Give the position of every Plasmodium falciparum parasite, noting its life-cycle stage.
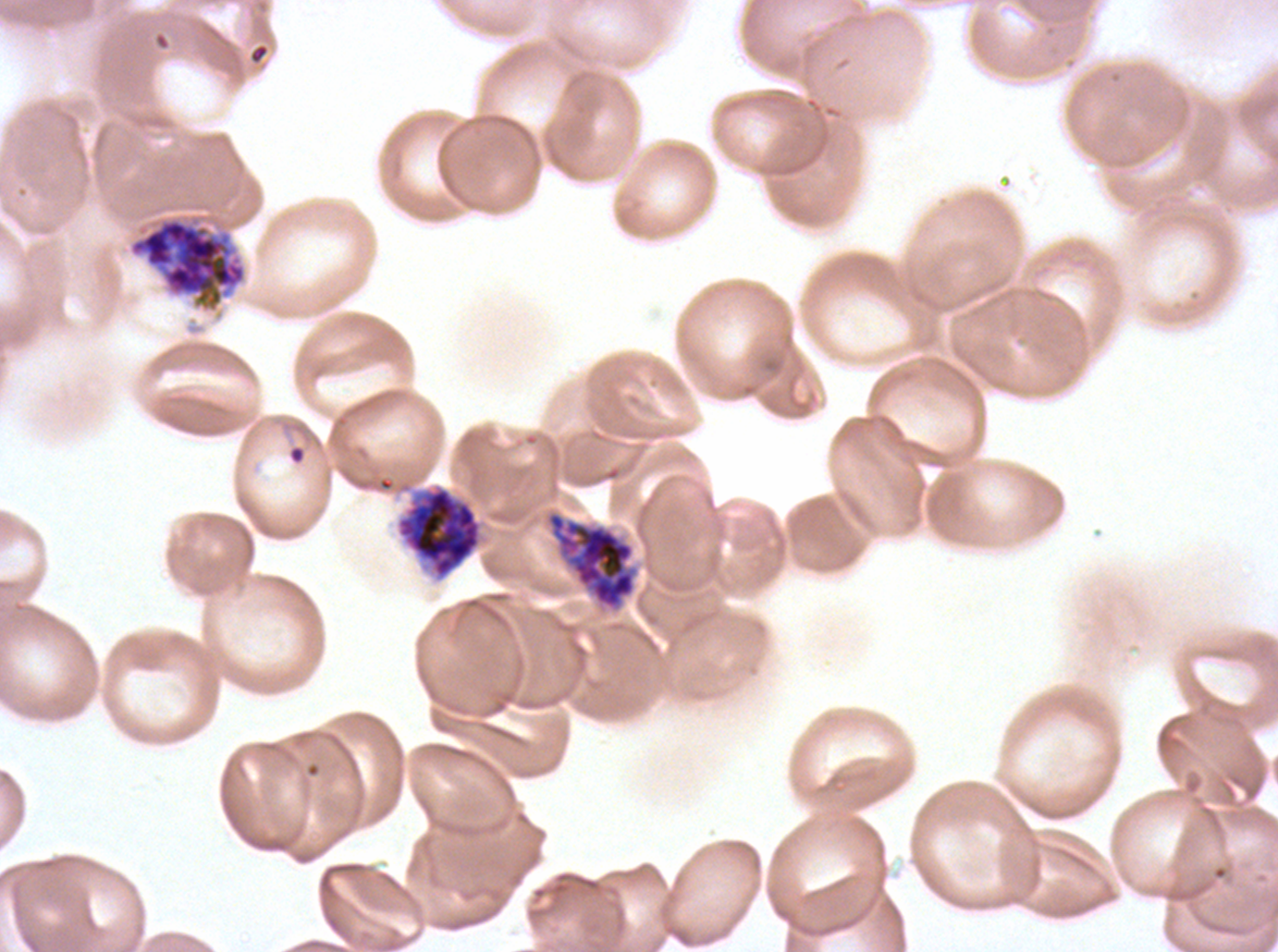
Approximate bounding boxes as {x1, y1, x2, y2} in pixels.
Rings: {289, 446, 305, 463}.
Early schizonts: {396, 486, 482, 580}.
Late schizonts: {128, 214, 247, 313}, {547, 512, 635, 609}.
No late-ring/early-trophozoite forms, mid trophozoites, late trophozoites, segmenters, or gametocytes observed.

Summary:
  - Stain: Giemsa
  - Life-cycle stages observed: ring, early schizont, late schizont
  - Image size: 1278×952 pixels
  - Specimen: ex-vivo Plasmodium falciparum culture from a patient in The Gambia, grown for 24 to 48 hours
  - Field of view: sub-image separated from a larger composite
  - Preparation: thin blood smear